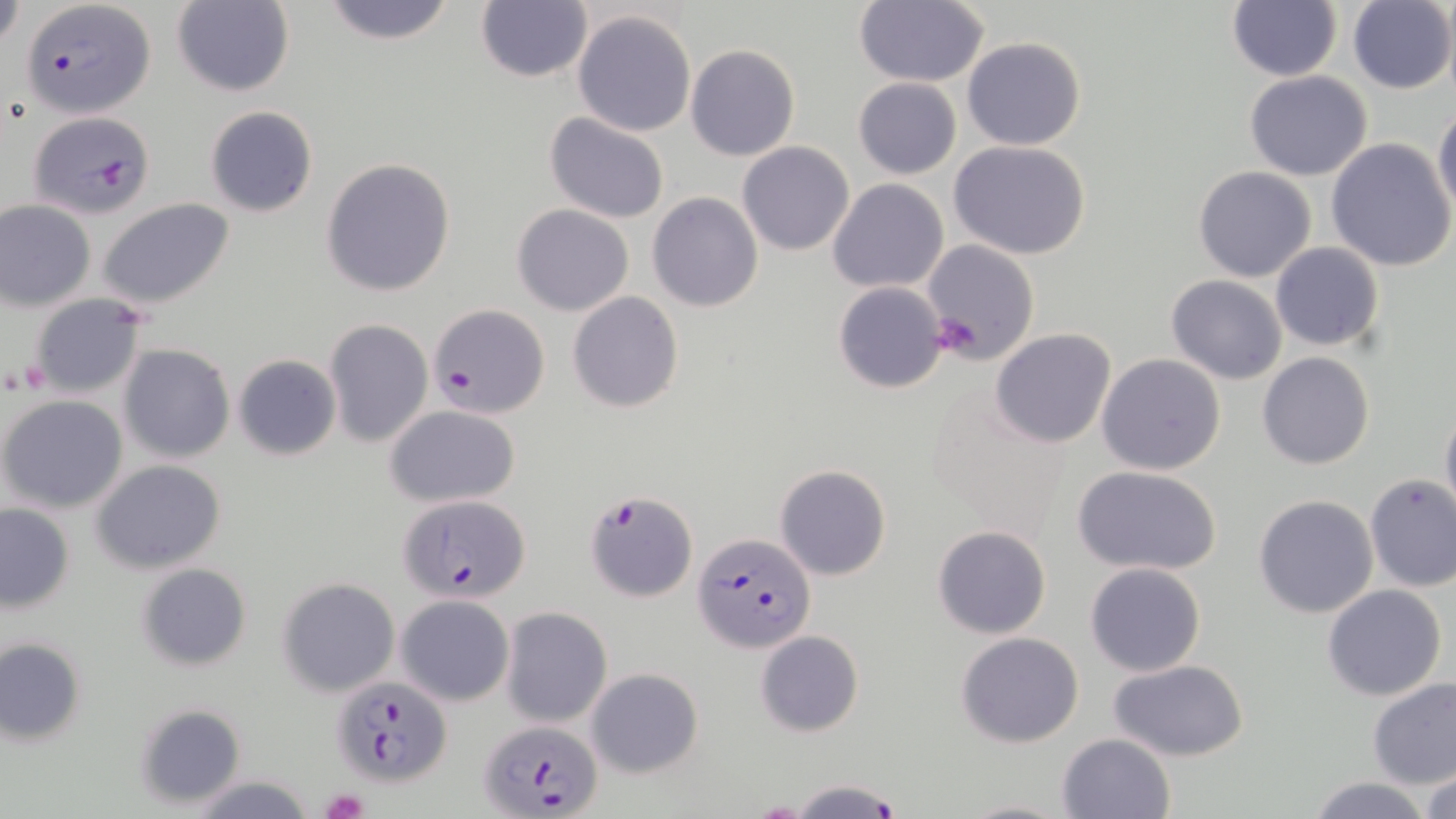
Approximate bounding boxes as [x1, y1, x2, y2] in pixels. Platelet locations: [929, 311, 985, 357], [320, 788, 368, 818]. Uninfected red blood cell locations: [172, 0, 294, 98], [1227, 0, 1342, 81], [0, 1, 24, 51], [319, 1, 460, 46], [476, 1, 593, 83], [852, 1, 989, 87], [1347, 2, 1455, 92], [571, 9, 696, 137], [961, 36, 1087, 151], [684, 43, 801, 161], [1244, 71, 1373, 180], [852, 78, 961, 180], [1434, 103, 1456, 217], [204, 105, 318, 217], [544, 112, 670, 224], [1327, 139, 1456, 272], [737, 141, 855, 255], [950, 141, 1092, 260], [321, 158, 456, 297], [1192, 166, 1318, 282], [827, 178, 948, 293], [648, 192, 763, 312], [0, 200, 95, 310], [98, 200, 234, 308], [513, 204, 634, 316], [921, 239, 1039, 364], [1269, 243, 1384, 351], [1166, 275, 1287, 385], [833, 281, 947, 392], [27, 292, 150, 401], [567, 292, 684, 412], [324, 318, 432, 447], [990, 329, 1116, 447], [118, 344, 235, 463], [1257, 352, 1374, 471], [1097, 353, 1226, 476], [233, 354, 340, 460], [1, 395, 129, 514], [1440, 401, 1456, 526], [385, 405, 521, 508], [92, 460, 226, 573], [774, 463, 891, 581], [1071, 465, 1221, 574], [1363, 474, 1456, 591], [1253, 494, 1379, 618], [0, 504, 74, 612], [933, 524, 1051, 639], [138, 561, 252, 670], [1084, 563, 1207, 677], [279, 578, 399, 696], [1321, 584, 1447, 701], [396, 595, 515, 705], [502, 607, 612, 726], [754, 630, 864, 736], [956, 632, 1084, 748], [1, 637, 87, 745], [1110, 660, 1249, 762], [586, 668, 704, 777], [1366, 678, 1456, 790], [135, 703, 246, 807], [1056, 733, 1175, 819], [1421, 763, 1456, 819], [185, 773, 314, 818], [1304, 776, 1435, 818], [955, 797, 1072, 818]. Plasmodium falciparum-infected red blood cell locations: [21, 0, 156, 119], [26, 112, 155, 217], [429, 303, 549, 418], [585, 490, 697, 602], [397, 494, 530, 603], [693, 531, 815, 652], [330, 675, 453, 787], [478, 716, 604, 817], [782, 778, 908, 819]. Slide-level diagnosis: Plasmodium falciparum. May-Grünwald-Giemsa stain. Thin blood smear. Image is 1456×819 pixels. Single field of view. Light microscopy. 1000x magnification.